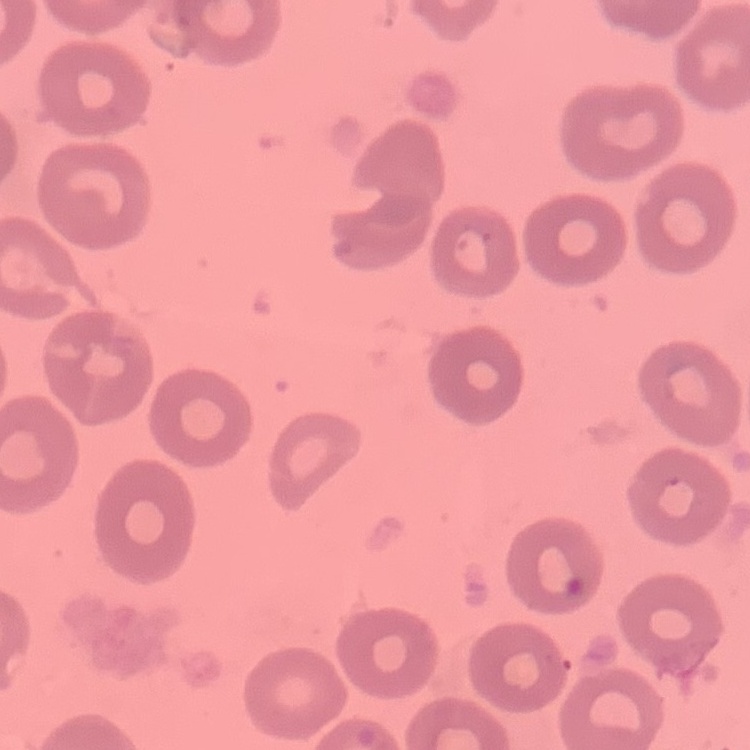
red blood cell morphology = no rouleaux formation
preparation = thin blood film
stain = Field's or Giemsa
image type = square crop of a larger photomicrograph